State which parasite is depicted.
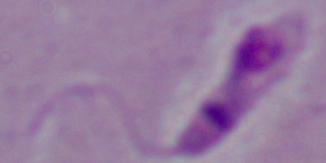

Leishmania.

modality = micrograph
magnification = 1000x